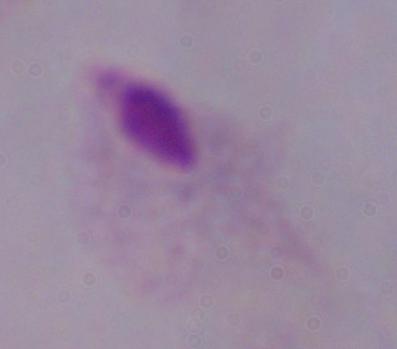

Summary:
  - Identification: trichomonad
  - Modality: photomicrograph
  - Magnification: 1000x